Give the position of every leukocyte visible.
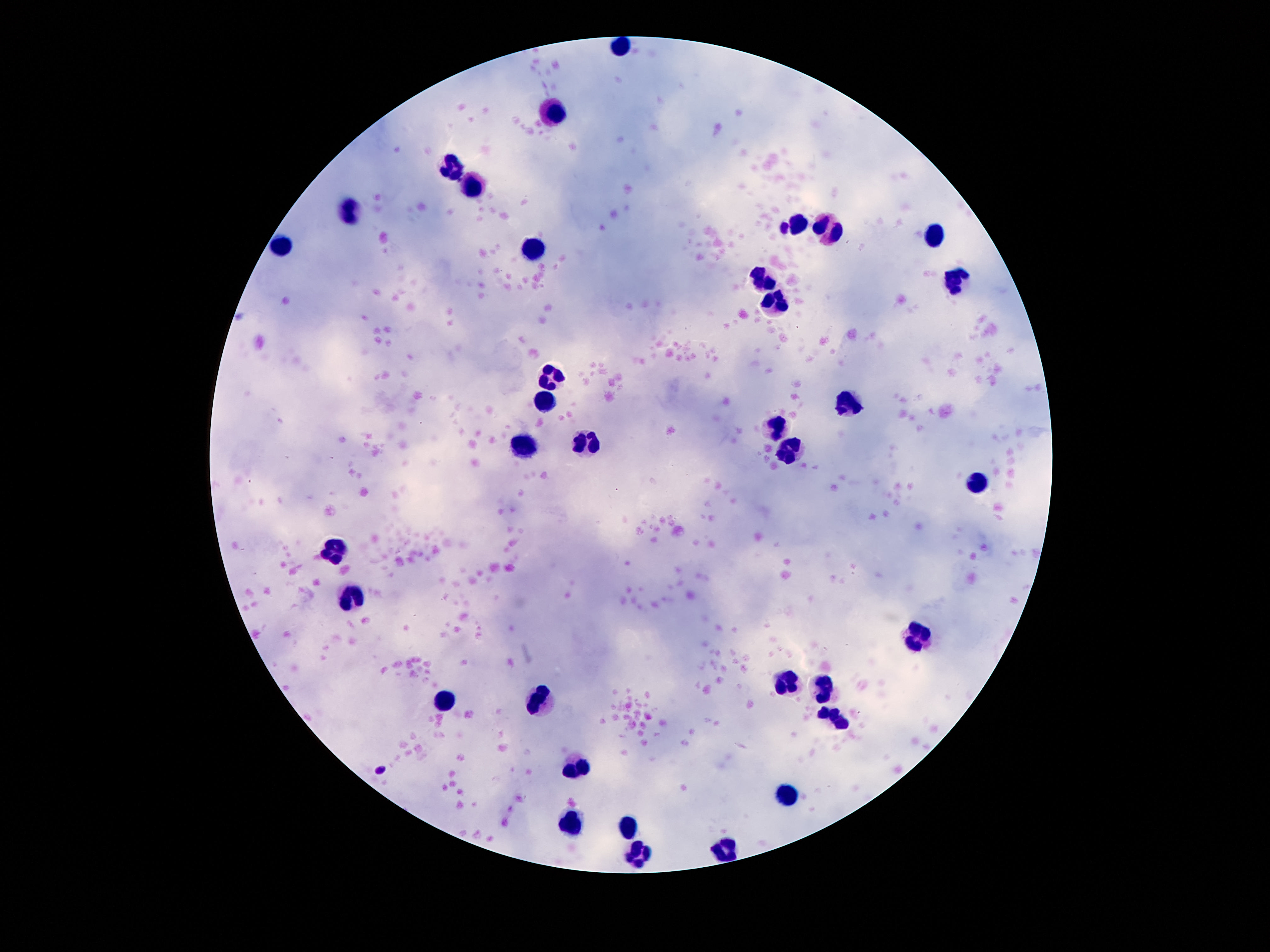
Approximate object centers, in pixels from the top-left corner.
Leukocytes: (x=621, y=46), (x=555, y=107), (x=453, y=172), (x=475, y=187), (x=352, y=211), (x=798, y=225), (x=834, y=230), (x=936, y=230), (x=282, y=247), (x=534, y=248), (x=954, y=280), (x=763, y=282), (x=777, y=302), (x=553, y=372), (x=545, y=397), (x=845, y=404), (x=773, y=427), (x=527, y=445), (x=591, y=447), (x=788, y=452), (x=977, y=482), (x=334, y=548), (x=352, y=591), (x=918, y=637), (x=786, y=680), (x=825, y=686), (x=443, y=702), (x=537, y=706), (x=838, y=722), (x=578, y=760), (x=789, y=798), (x=571, y=827), (x=627, y=830), (x=636, y=852), (x=720, y=852).

One field from this slide. 100x magnification. Patient malaria status: negative. Thick blood film. Giemsa stain. Smartphone photograph taken through the microscope eyepiece. Image is 1270×952 pixels.